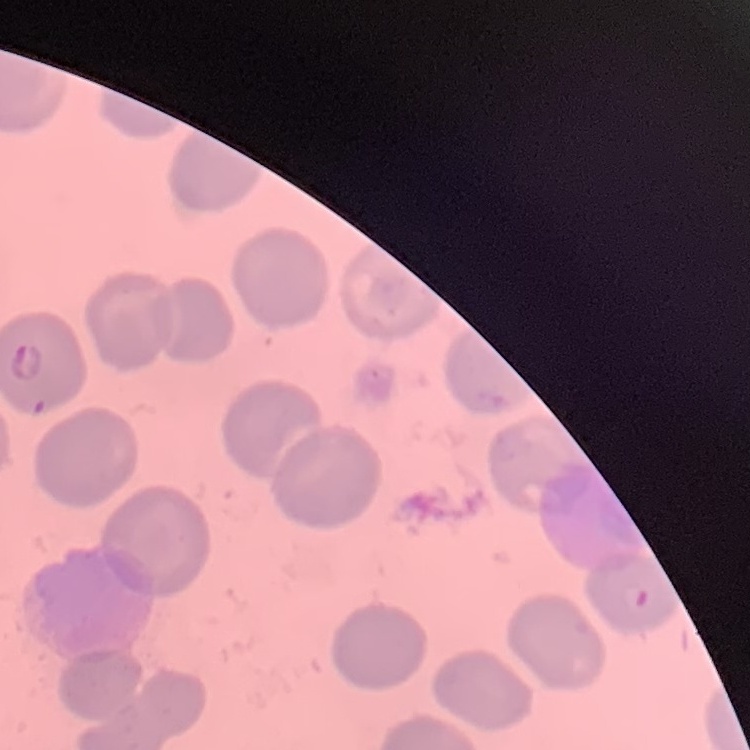
The erythrocytes exhibit no rouleaux formation. Square crop of a larger photomicrograph. Field's or Giemsa stain. Thin blood film.